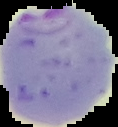 Cell region segmented out of the field of view; the surrounding area is masked to black. From a thin blood film. Malaria status: parasitized. Image is 118×127 pixels.